State the preparation type.
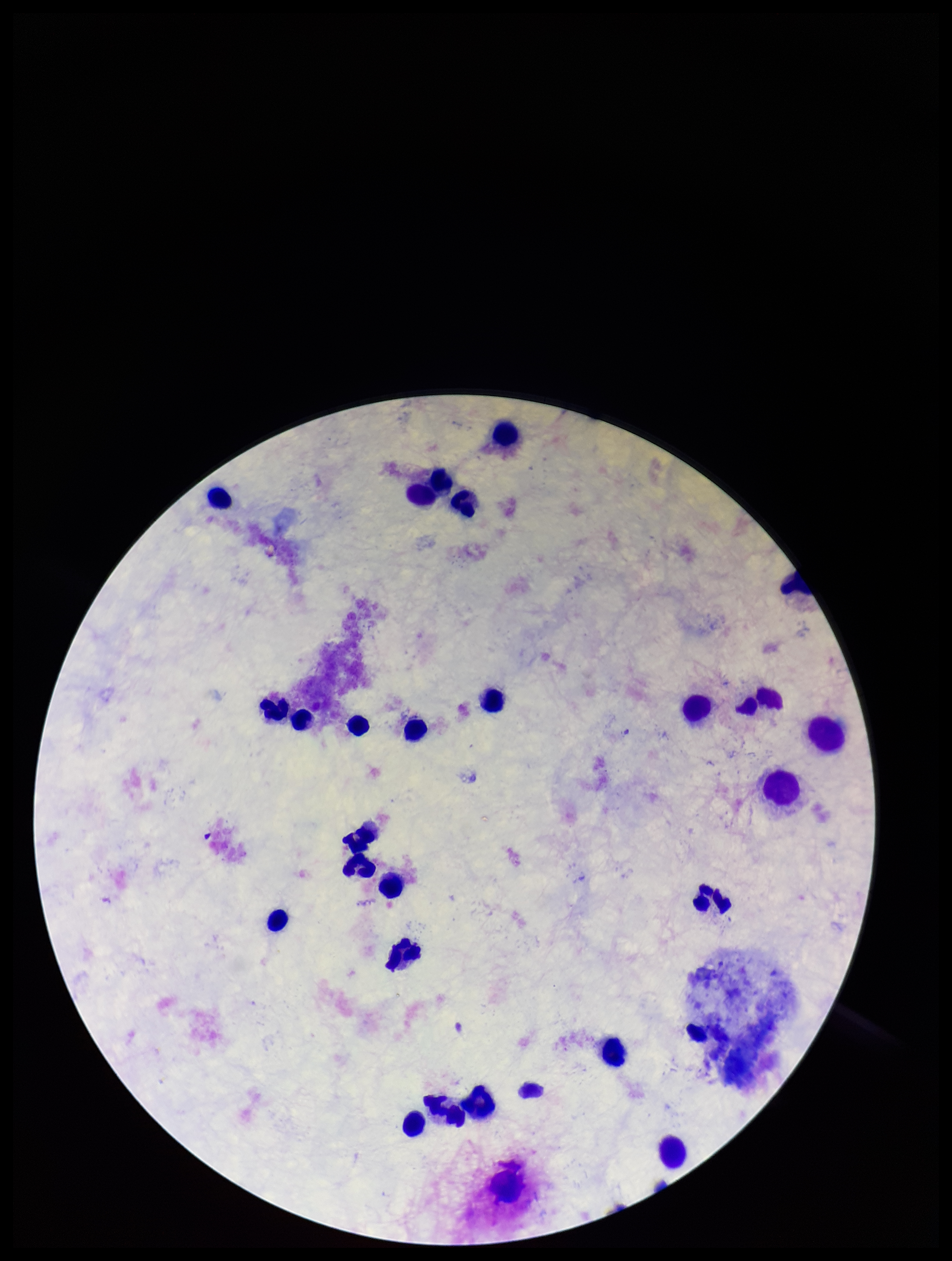

Thick.

Photographed through the microscope eyepiece with a smartphone camera. Image is 952×1261 pixels. Leukocyte count: 27. Plasmodium parasites: none seen. One field from this slide. Patient malaria status: negative. Parasite count: 0. Giemsa stain.